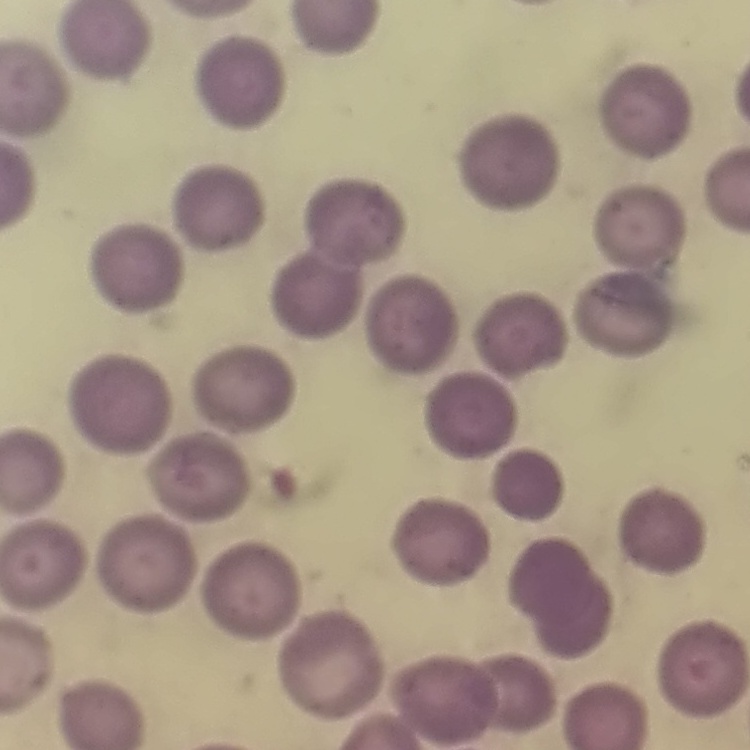
red_blood_cell_morphology: no rouleaux formation
stain: Field's or Giemsa
image_type: square crop of a larger photomicrograph
preparation: thin peripheral smear